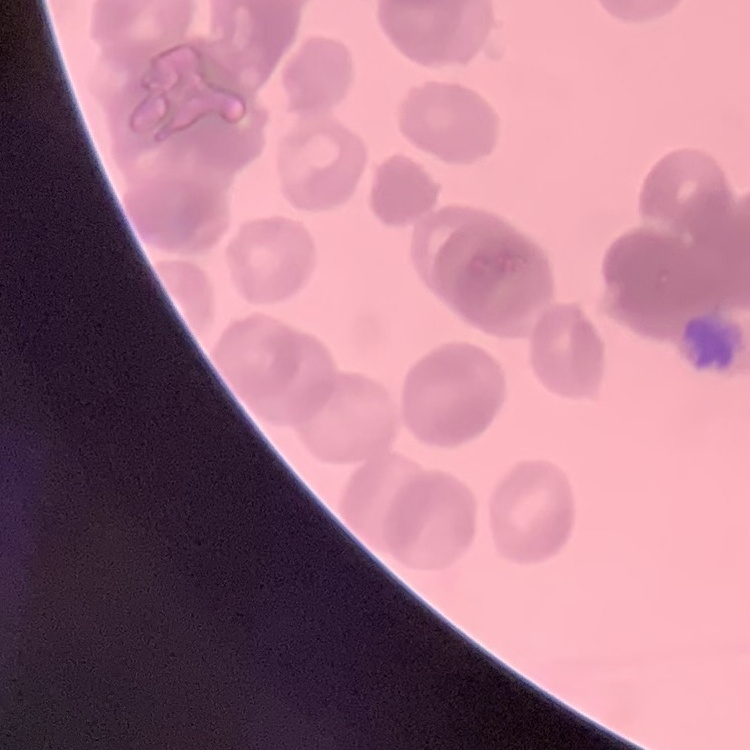

Summary:
  - Erythrocyte morphology: rouleaux formation
  - Image type: one tile cut from a larger photomicrograph
  - Preparation: thin peripheral smear
  - Stain: Field's or Giemsa